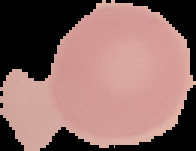 Cell region segmented out of the field of view; the surrounding area is masked to black. Image is 196×151 pixels. Malaria status: uninfected. From a thin blood film.